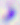
identification: Toxoplasma gondii
modality: photomicrograph
magnification: 400x